Give the position of every malaria parasite.
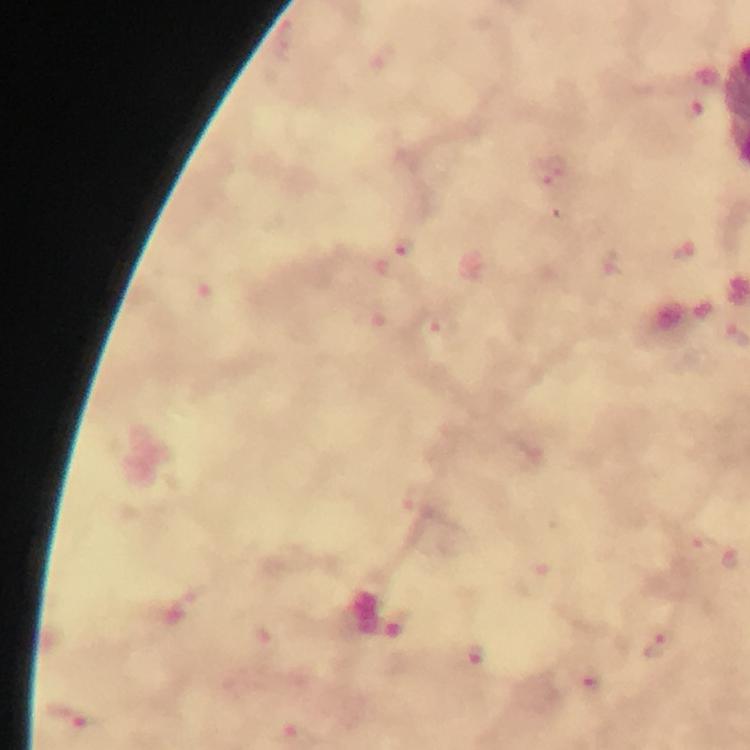

Approximate object centers, in pixels from the top-left corner.
Malaria parasites: (x=699, y=546), (x=729, y=557), (x=396, y=615), (x=663, y=645), (x=483, y=661).

cropped_from: one field of view
stain: Giemsa
preparation: thick blood film
context: from a diagnostic examination for malaria
magnification: 100x
immersion_oil: used
capture: smartphone mounted on the microscope
image_size: 750×750 pixels